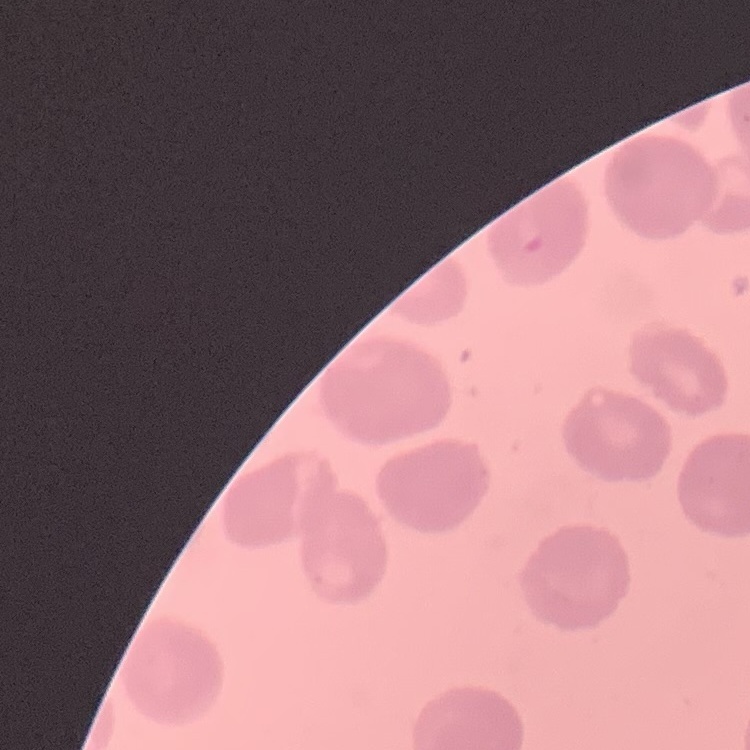

{
  "red_blood_cell_morphology": "no rouleaux formation",
  "preparation": "thin peripheral smear",
  "image_type": "one tile cut from a larger photomicrograph",
  "stain": "Field's or Giemsa"
}